State which parasite is depicted.
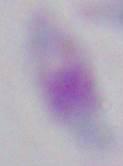
Toxoplasma gondii.

Summary:
  - Magnification: 1000x
  - Modality: micrograph